Identify the parasite.
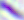
Toxoplasma gondii.

Summary:
  - Modality: micrograph
  - Magnification: 400x